Report the malaria status of this cell.
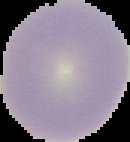

It is uninfected.

preparation: thin blood smear
image_type: cell region segmented out of the field of view; surrounding area masked to black
image_size: 130×142 pixels